Give the extent of all Plasmodium falciparum-infected red blood cells.
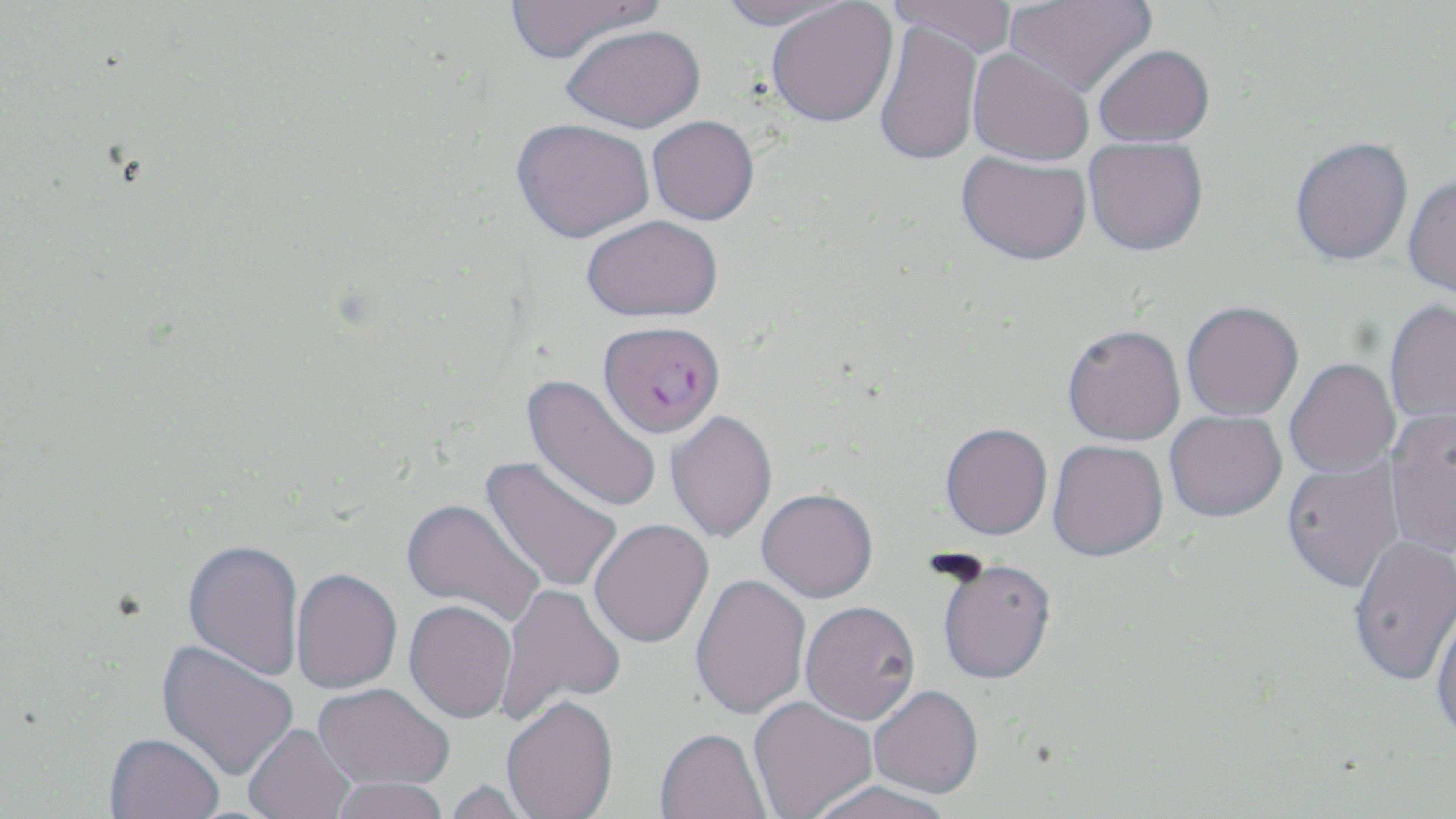
Approximate bounding boxes as named x1/y1/x2/y2 corners in pixels.
Plasmodium falciparum-infected red blood cells: (x1=599, y1=321, x2=726, y2=438).

slide-level diagnosis = Plasmodium falciparum
image size = 1456×819 pixels
stain = May-Grünwald-Giemsa
modality = light microscopy
preparation = thin blood film
magnification = 1000x
field of view = one of a larger specimen
uninfected red blood cell locations = approximate bounding boxes as named x1/y1/x2/y2 corners in pixels: (x1=506, y1=0, x2=663, y2=63), (x1=717, y1=0, x2=858, y2=30), (x1=1004, y1=0, x2=1156, y2=97), (x1=766, y1=1, x2=898, y2=127), (x1=887, y1=1, x2=1019, y2=57), (x1=874, y1=20, x2=984, y2=166), (x1=562, y1=24, x2=706, y2=133), (x1=1093, y1=44, x2=1215, y2=146), (x1=967, y1=47, x2=1094, y2=165), (x1=647, y1=115, x2=759, y2=225), (x1=512, y1=118, x2=655, y2=242), (x1=1290, y1=136, x2=1413, y2=264), (x1=1084, y1=137, x2=1208, y2=255), (x1=957, y1=151, x2=1092, y2=265), (x1=1403, y1=173, x2=1456, y2=299), (x1=582, y1=215, x2=723, y2=322), (x1=1384, y1=299, x2=1456, y2=426), (x1=1181, y1=301, x2=1304, y2=420), (x1=1062, y1=323, x2=1185, y2=446), (x1=1285, y1=358, x2=1400, y2=479), (x1=521, y1=373, x2=662, y2=515), (x1=1385, y1=409, x2=1456, y2=559), (x1=1165, y1=410, x2=1287, y2=521), (x1=666, y1=411, x2=778, y2=544), (x1=940, y1=422, x2=1052, y2=540), (x1=1048, y1=439, x2=1168, y2=562), (x1=479, y1=456, x2=623, y2=593), (x1=1282, y1=457, x2=1405, y2=592), (x1=756, y1=491, x2=878, y2=605), (x1=401, y1=498, x2=544, y2=626), (x1=589, y1=521, x2=715, y2=650), (x1=1349, y1=535, x2=1456, y2=686), (x1=183, y1=540, x2=305, y2=681), (x1=938, y1=563, x2=1056, y2=687), (x1=291, y1=569, x2=402, y2=695), (x1=691, y1=575, x2=812, y2=721), (x1=495, y1=582, x2=626, y2=719), (x1=1431, y1=600, x2=1456, y2=745), (x1=403, y1=602, x2=517, y2=725), (x1=801, y1=604, x2=921, y2=728), (x1=155, y1=639, x2=299, y2=782), (x1=313, y1=685, x2=454, y2=793), (x1=869, y1=688, x2=983, y2=801), (x1=748, y1=698, x2=877, y2=819), (x1=502, y1=699, x2=619, y2=819), (x1=244, y1=724, x2=357, y2=819), (x1=654, y1=731, x2=772, y2=819), (x1=104, y1=734, x2=224, y2=819), (x1=329, y1=779, x2=450, y2=819), (x1=441, y1=781, x2=539, y2=819), (x1=807, y1=783, x2=951, y2=819)